Report the malaria status of this cell.
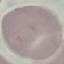
It is uninfected.

Thin blood film. Automatically extracted cell patch, resized to 64 × 64 pixels. Photographed with a smartphone camera at the microscope eyepiece. Giemsa-stained preparation.